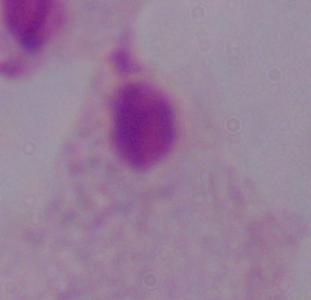

magnification = 1000x
modality = micrograph
identification = trichomonad